Report the malaria status.
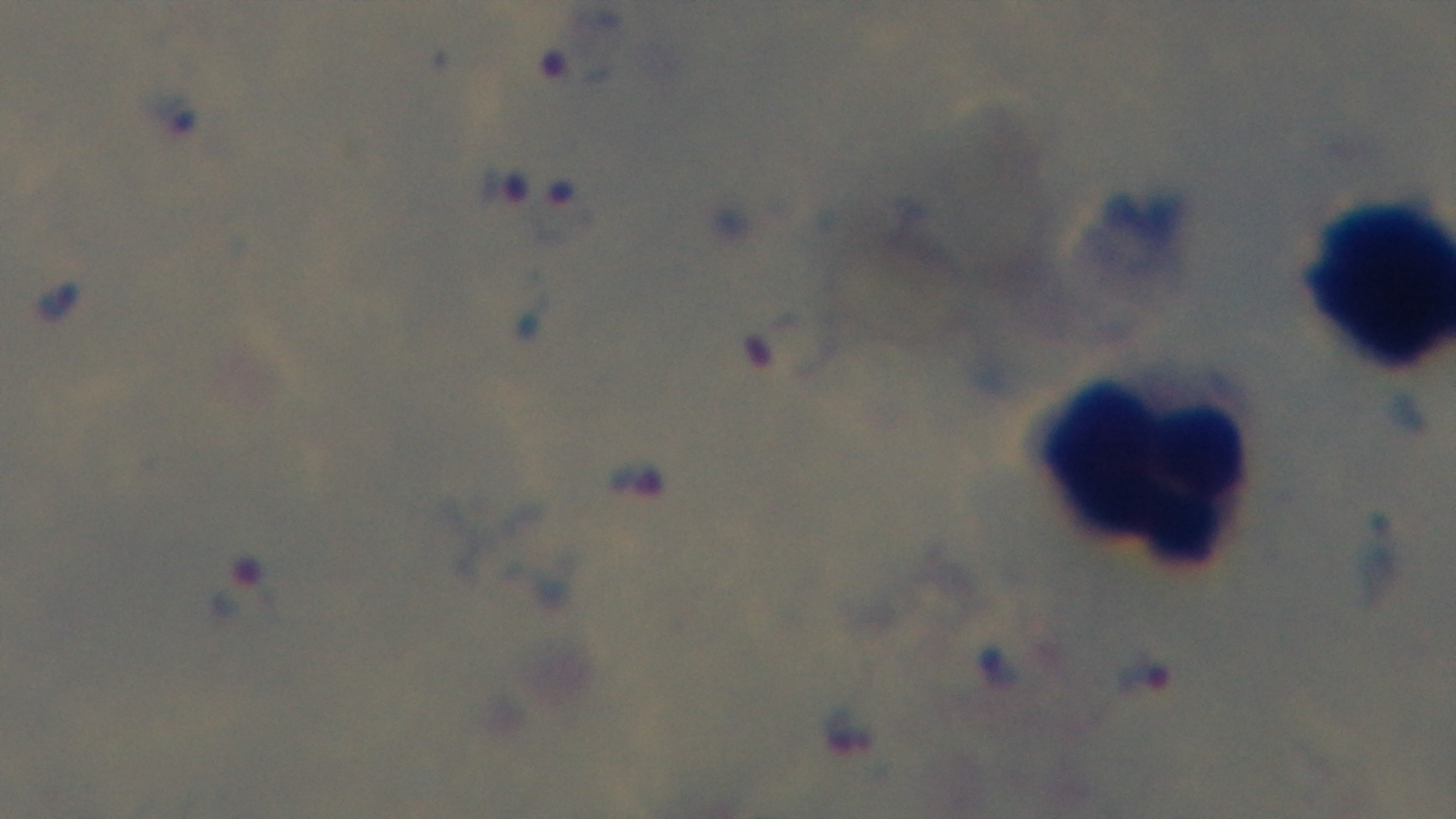
It is infected.

Summary:
  - Field of view: one from the slide
  - Preparation: thick smear
  - Stain: Giemsa
  - Capture: mounted 4K digital camera
  - Modality: light microscopy
  - Objective: 100x oil immersion